Describe the morphology of the erythrocytes.
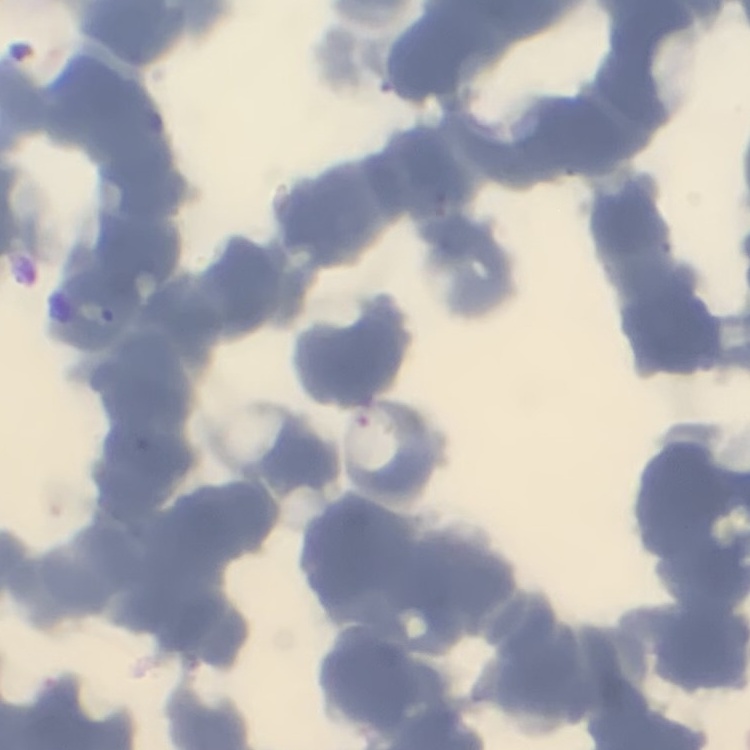
They show rouleaux formation.

Summary:
  - Image type: one tile cut from a larger photomicrograph
  - Preparation: thin blood smear
  - Stain: Field's or Giemsa